State which cell type is depicted.
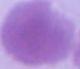

This is an erythrocyte.

Photomicrograph. Captured at 1000x magnification.